Give the position of every Plasmodium parasite visible.
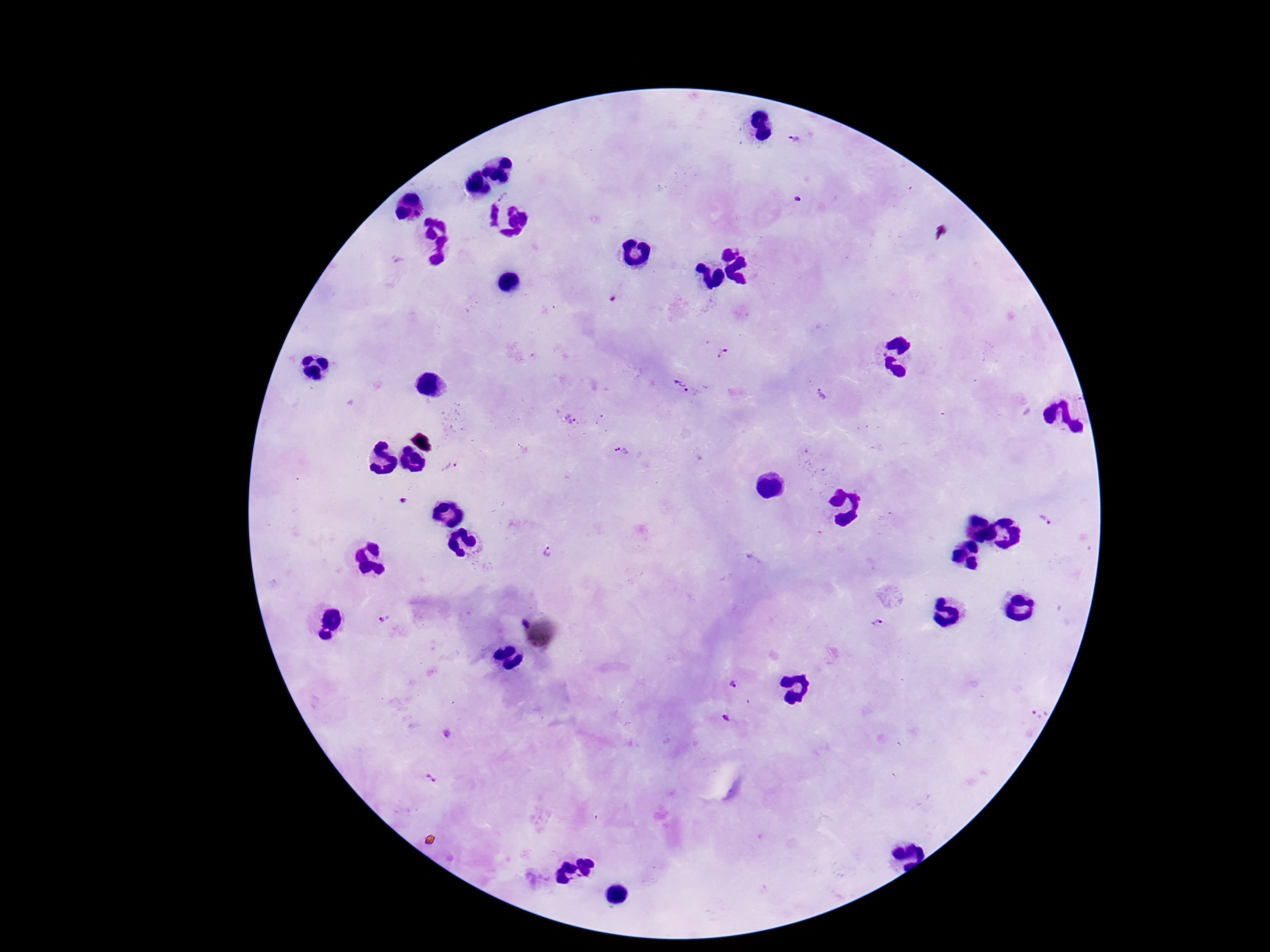
Approximate centers as (x, y) in pixels.
Plasmodium parasites: (794, 140), (501, 195), (798, 199), (726, 354), (680, 385), (819, 394), (568, 419), (620, 452), (450, 467), (1044, 521), (548, 554), (383, 621), (882, 623), (734, 687), (1039, 714), (728, 717), (446, 732), (430, 776).

image size = 1270×952 pixels
field of view = single
magnification = 100x
capture = smartphone camera through the microscope eyepiece
stain = Giemsa
patient malaria status = infected
preparation = thick peripheral-blood smear